Locate and identify every blood parasite.
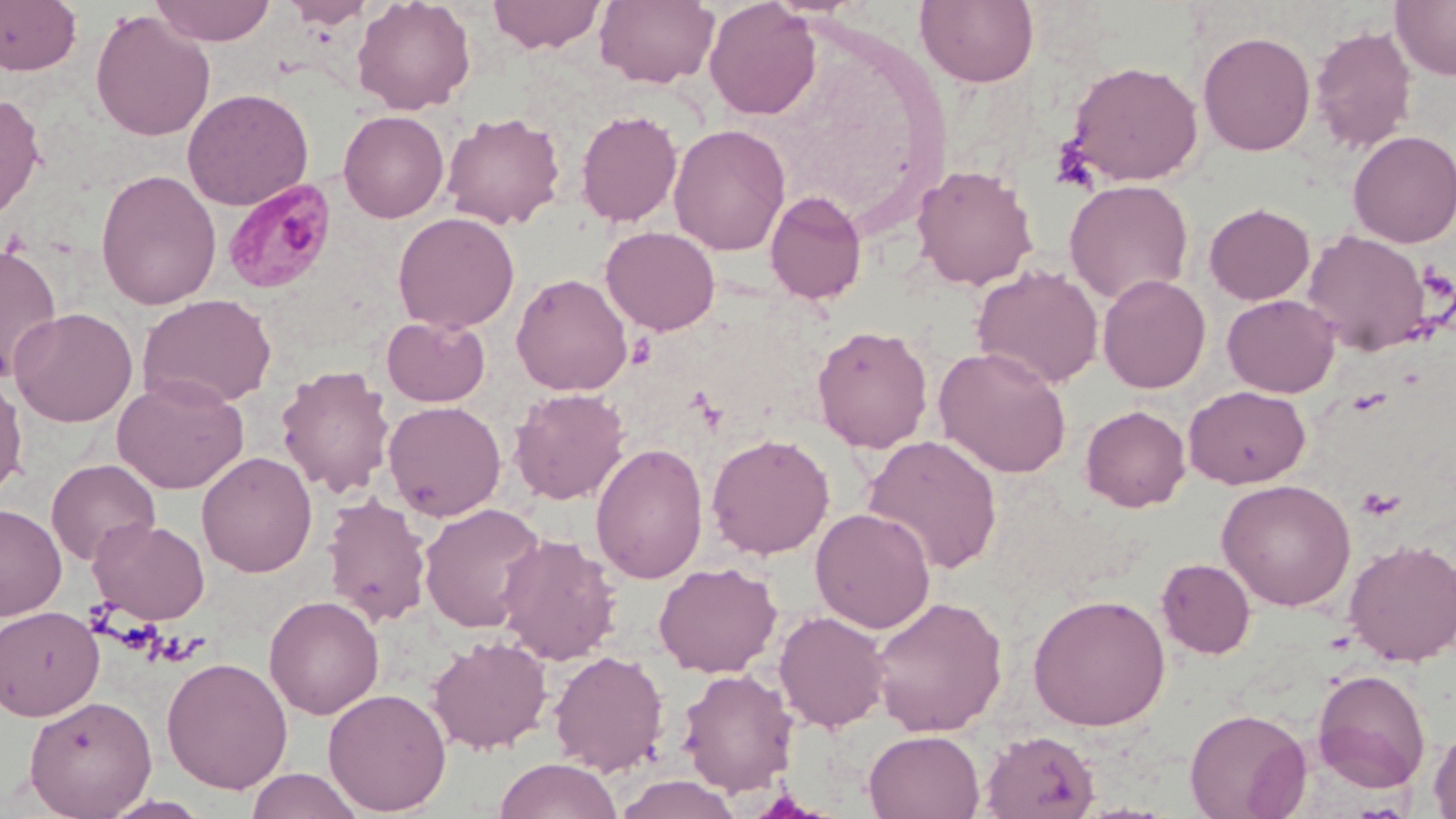

Approximate bounding boxes as (x1,y1)-(x2,y2) corner pairs in pixels.
Plasmodium malariae-infected red blood cells: (222,178)-(338,294).
No Plasmodium falciparum, Plasmodium ovale, Plasmodium vivax, Babesia divergens, or Trypanosoma brucei observed.

Uninfected red blood cell locations: (0,0)-(82,76), (150,0)-(276,46), (283,0)-(373,29), (351,0)-(476,115), (487,0)-(608,54), (594,0)-(719,88), (704,0)-(821,120), (915,0)-(1040,88), (1391,0)-(1456,81), (90,9)-(216,142), (1309,25)-(1417,154), (1197,30)-(1316,156), (1064,59)-(1204,186), (182,87)-(314,211), (0,92)-(46,223), (575,108)-(683,228), (338,110)-(450,223), (441,111)-(566,230), (669,123)-(791,256), (1348,129)-(1456,248), (911,164)-(1039,291), (95,169)-(221,310), (1064,179)-(1193,305), (765,190)-(868,305), (1204,202)-(1315,305), (392,211)-(520,334), (601,226)-(721,335), (1301,230)-(1433,355), (0,242)-(63,382), (971,264)-(1104,391), (511,272)-(633,395), (1097,274)-(1211,394), (138,293)-(277,410), (1222,293)-(1340,397), (9,307)-(138,427), (381,316)-(491,407), (811,324)-(934,453), (933,346)-(1073,478), (275,364)-(395,497), (0,373)-(28,500), (112,375)-(249,493), (1183,385)-(1311,489), (508,388)-(630,505), (383,400)-(506,521), (1080,404)-(1191,512), (706,433)-(835,560), (862,434)-(1004,575), (590,442)-(709,584), (196,451)-(318,577), (46,458)-(160,567), (1216,479)-(1356,611), (322,493)-(432,627), (419,502)-(548,633), (0,503)-(66,621), (811,507)-(936,634), (89,517)-(210,625), (496,533)-(622,665), (1344,538)-(1456,666), (1156,558)-(1257,659), (653,561)-(782,678), (1028,593)-(1171,731), (263,594)-(384,720), (869,594)-(1007,736), (0,605)-(104,720), (774,610)-(891,732), (426,634)-(552,754), (548,650)-(670,776), (161,656)-(293,794), (677,668)-(798,796), (1312,668)-(1431,792), (323,688)-(452,815), (24,695)-(157,817), (1184,707)-(1312,819), (1428,724)-(1456,819), (864,730)-(985,819), (979,730)-(1101,818), (494,757)-(623,819), (244,768)-(364,819), (612,774)-(745,818), (100,794)-(213,818). Platelet locations: (1050,140)-(1098,191). Slide-level diagnosis: Plasmodium malariae. May-Grünwald-Giemsa stain. Captured at 1000x magnification. Optical microscopy. One field of a larger specimen. Thin blood smear. Image is 1456×819 pixels.